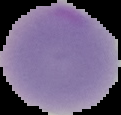
From a thin blood film. Image is 121×115 pixels. Result: no malaria parasites seen. Segmented cell region on a black background.